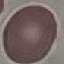 Malaria status: uninfected. Acquired by smartphone through the microscope eyepiece. Giemsa stain. Thin blood film. Automatically extracted cell patch, resized to 64 × 64 pixels.